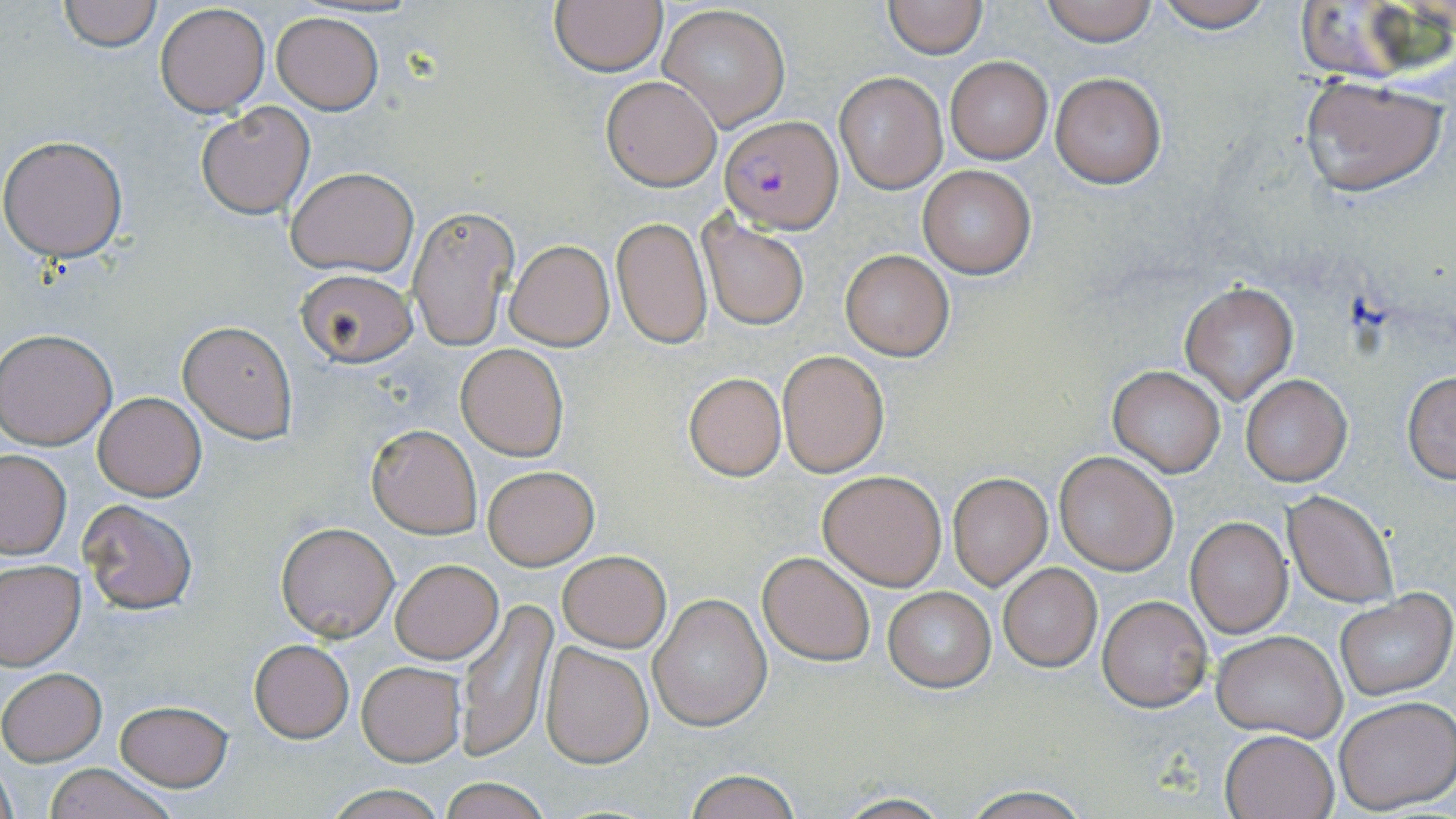 Approximate bounding boxes as (x1,y1)-(x2,y2) corner pairs in pixels. Plasmodium falciparum-infected red blood cell locations: (722,115)-(843,232). Uninfected red blood cell locations: (58,0)-(159,50), (549,0)-(667,76), (1038,0)-(1161,46), (1149,0)-(1277,31), (1291,0)-(1444,85), (881,1)-(987,58), (155,2)-(271,116), (656,4)-(791,132), (272,11)-(384,113), (944,56)-(1053,164), (1049,70)-(1168,188), (835,73)-(945,192), (601,74)-(722,191), (1298,76)-(1445,197), (195,102)-(315,219), (0,133)-(130,262), (918,166)-(1036,277), (286,167)-(418,276), (408,205)-(518,351), (612,217)-(712,349), (698,217)-(808,331), (505,240)-(613,350), (840,250)-(954,360), (294,269)-(418,368), (1179,282)-(1298,403), (178,319)-(299,441), (1,328)-(117,449), (456,343)-(569,461), (779,351)-(887,476), (1108,365)-(1225,477), (683,372)-(786,481), (1402,373)-(1455,484), (1241,374)-(1350,485), (93,392)-(207,501), (367,425)-(482,538), (0,450)-(72,559), (1054,452)-(1178,573), (483,466)-(598,569), (817,470)-(947,590), (948,474)-(1050,590), (1284,490)-(1398,608), (79,499)-(198,615), (1186,517)-(1292,638), (274,521)-(399,643), (557,550)-(671,652), (758,551)-(875,666), (390,559)-(503,663), (0,561)-(85,669), (998,563)-(1101,671), (883,586)-(995,691), (1334,589)-(1455,699), (650,593)-(771,731), (456,596)-(558,758), (1098,596)-(1210,712), (1212,630)-(1346,742), (249,638)-(353,742), (540,641)-(653,767), (355,660)-(465,766), (0,667)-(106,765), (1333,695)-(1456,812), (113,699)-(234,789), (1220,728)-(1340,819), (41,764)-(180,819), (682,770)-(805,819), (439,777)-(552,819), (320,784)-(452,819), (959,787)-(1097,819), (826,793)-(957,819). Slide-level diagnosis: Plasmodium falciparum. Optical microscopy. Single field of view. Captured at 1000x magnification. Thin blood smear. May-Grünwald-Giemsa stain. Image is 1456×819 pixels.